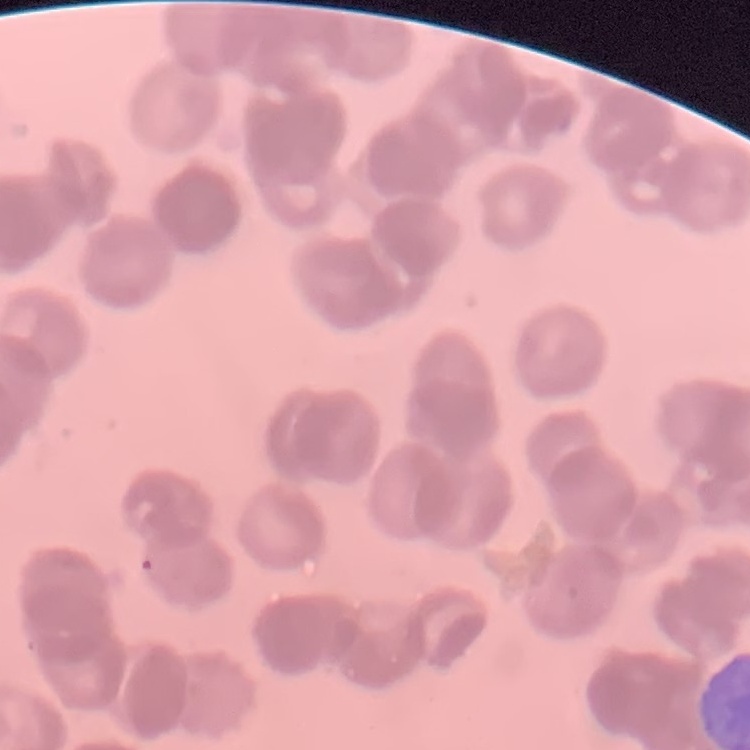
{
  "erythrocyte_morphology": "rouleaux formation",
  "image_type": "one tile cut from a larger photomicrograph",
  "stain": "Field's or Giemsa",
  "preparation": "thin blood film"
}